Assess this cell for malaria.
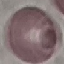

It is uninfected.

{
  "preparation": "thin smear",
  "capture": "smartphone through the microscope eyepiece",
  "image_type": "cell patch, automatically extracted from a larger field of view and resized to 64 × 64 pixels",
  "stain": "Giemsa"
}